Identify the parasite.
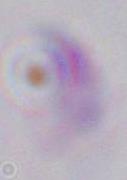
Toxoplasma gondii.

{
  "modality": "photomicrograph",
  "magnification": "1000x"
}